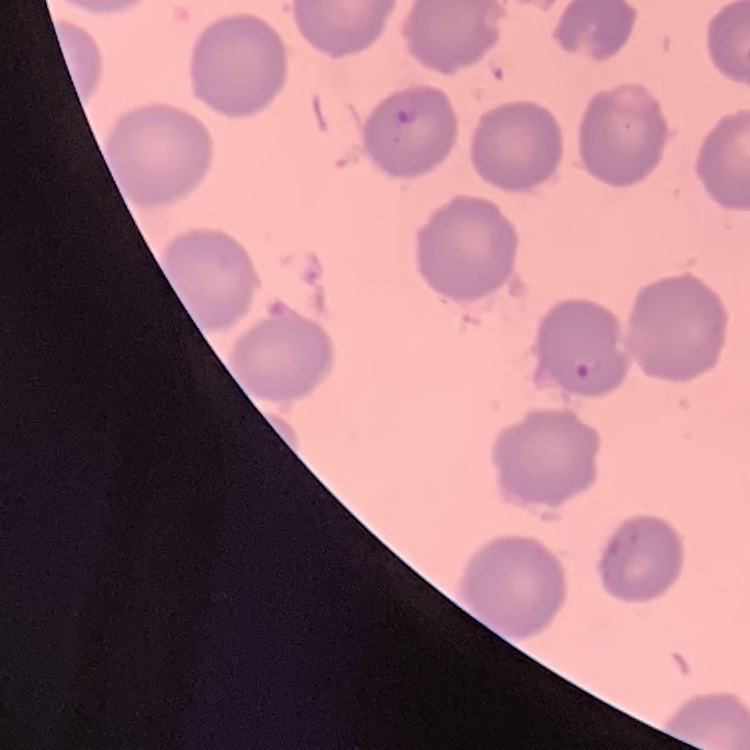

erythrocyte morphology = no rouleaux formation
preparation = thin peripheral smear
image type = one tile cut from a larger photomicrograph
stain = Field's or Giemsa